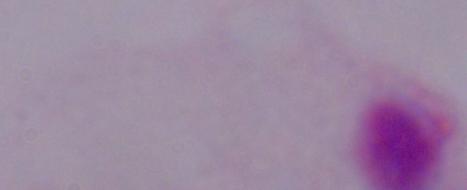 A trichomonad is shown. Captured at 1000x magnification. Micrograph.